Classify this cell by malaria status.
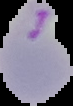

It is parasitized.

Image is 73×106 pixels. Segmented cell region on a black background. From a thin blood film.